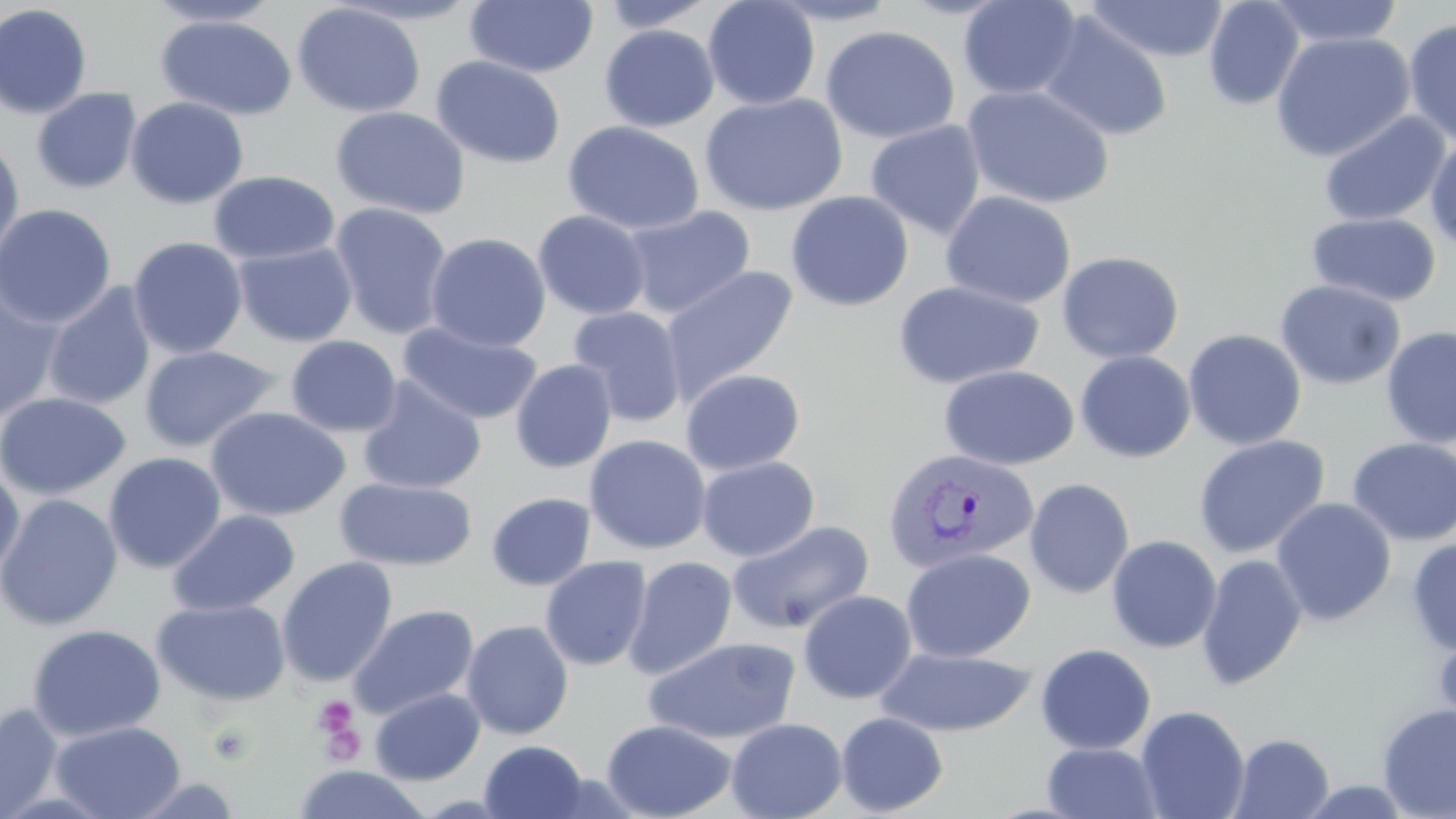
Summary:
  - Coordinate format: approximate bounding boxes as (x1, y1, x2, y2) in pixels
  - Platelet locations: (312, 695, 364, 757), (207, 721, 257, 767)
  - Plasmodium vivax-infected red blood cell locations: (882, 446, 1039, 574)
  - Uninfected red blood cell locations: (702, 0, 821, 110), (765, 0, 903, 25), (957, 0, 1083, 100), (1203, 0, 1305, 111), (1266, 0, 1405, 48), (143, 1, 283, 27), (328, 1, 485, 26), (464, 1, 599, 78), (594, 1, 720, 32), (1083, 1, 1230, 63), (292, 2, 426, 118), (0, 4, 93, 119), (1038, 12, 1173, 142), (156, 15, 297, 120), (1402, 18, 1456, 148), (599, 25, 719, 132), (820, 25, 960, 144), (1271, 31, 1415, 162), (431, 55, 566, 169), (962, 84, 1116, 209), (31, 87, 142, 195), (698, 93, 848, 217), (125, 97, 248, 209), (330, 106, 470, 219), (1318, 111, 1450, 227), (562, 120, 704, 235), (865, 120, 986, 240), (1425, 132, 1456, 255), (0, 137, 25, 269), (208, 170, 340, 265), (785, 191, 914, 312), (940, 191, 1076, 309), (328, 202, 453, 339), (0, 203, 116, 329), (622, 206, 756, 320), (533, 210, 651, 320), (1306, 212, 1442, 307), (426, 232, 551, 352), (128, 237, 248, 360), (233, 241, 357, 347), (1056, 250, 1185, 364), (661, 265, 798, 404), (1275, 279, 1405, 390), (892, 280, 1044, 389), (42, 283, 157, 411), (0, 284, 66, 423), (567, 306, 688, 427), (398, 322, 542, 425), (1380, 325, 1456, 448), (1183, 329, 1306, 451), (285, 335, 402, 437), (139, 345, 282, 453), (1074, 351, 1196, 463), (510, 360, 617, 473), (938, 365, 1079, 471), (680, 368, 805, 475), (356, 377, 486, 495), (0, 392, 131, 500), (206, 407, 351, 521), (584, 434, 711, 555), (1193, 435, 1330, 558), (1346, 437, 1456, 546), (103, 452, 227, 573), (696, 456, 820, 562), (0, 465, 25, 580), (335, 478, 477, 570), (1024, 478, 1135, 599), (486, 492, 596, 591), (0, 494, 123, 631), (1270, 497, 1397, 626), (167, 509, 300, 617), (726, 520, 874, 635), (1105, 535, 1222, 653), (1406, 537, 1456, 656), (900, 548, 1035, 663), (1196, 554, 1308, 691), (277, 556, 397, 686), (540, 556, 652, 671), (623, 556, 738, 680), (797, 589, 917, 704), (152, 598, 290, 706), (348, 604, 479, 720), (461, 619, 574, 739), (26, 623, 166, 742), (1432, 626, 1456, 743), (643, 636, 801, 745), (1035, 643, 1156, 754), (876, 645, 1036, 737), (369, 687, 485, 785), (0, 702, 64, 818), (1376, 703, 1456, 819), (1135, 705, 1250, 819), (836, 712, 948, 816), (725, 717, 847, 819), (601, 718, 737, 819), (49, 720, 186, 819), (1229, 733, 1335, 819), (479, 740, 589, 819), (1042, 742, 1164, 819), (291, 764, 434, 819), (128, 775, 242, 817)
  - Slide-level diagnosis: Plasmodium vivax
  - Stain: May-Grünwald-Giemsa
  - Image size: 1456×819 pixels
  - Modality: light microscopy
  - Magnification: 1000x
  - Preparation: thin blood smear
  - Field of view: one of a larger specimen